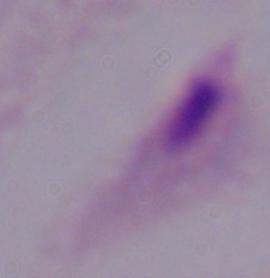

{
  "modality": "micrograph",
  "magnification": "1000x",
  "identification": "trichomonad"
}